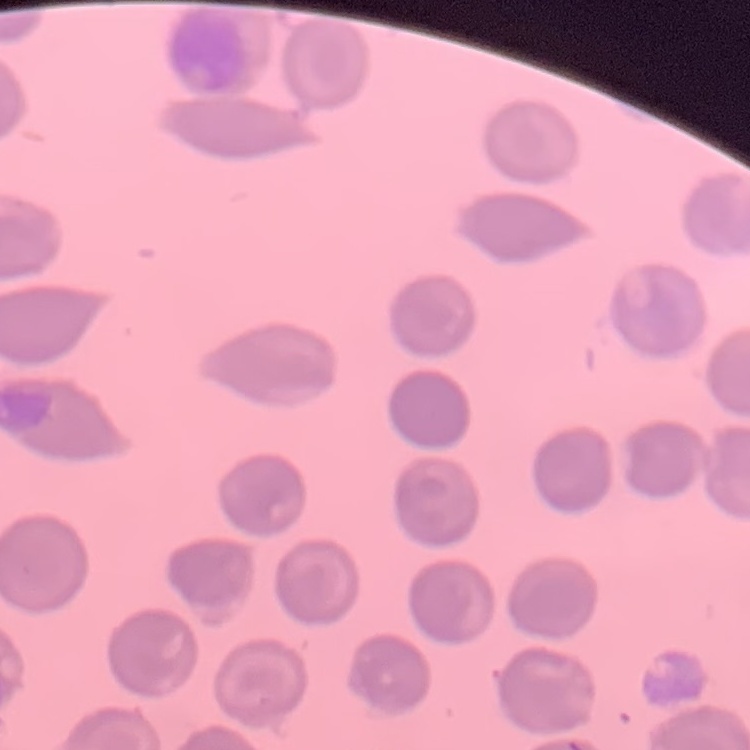
red blood cell morphology = no rouleaux formation
preparation = thin peripheral smear
image type = square crop of a larger photomicrograph
stain = Field's or Giemsa